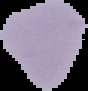
Segmented cell region on a black background. From a thin blood smear. Image is 88×91 pixels. Result: no malaria parasites seen.